Report the malaria status of this cell.
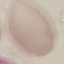

Uninfected.

capture = smartphone through the microscope eyepiece
stain = Giemsa
image type = automatically extracted cell patch, resized to 64 × 64 pixels
preparation = thin blood smear